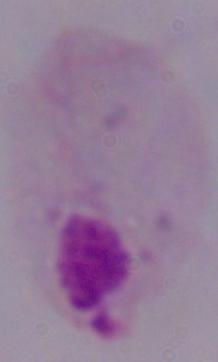

Summary:
  - Magnification: 1000x
  - Modality: micrograph
  - Identification: trichomonad